Locate platelets.
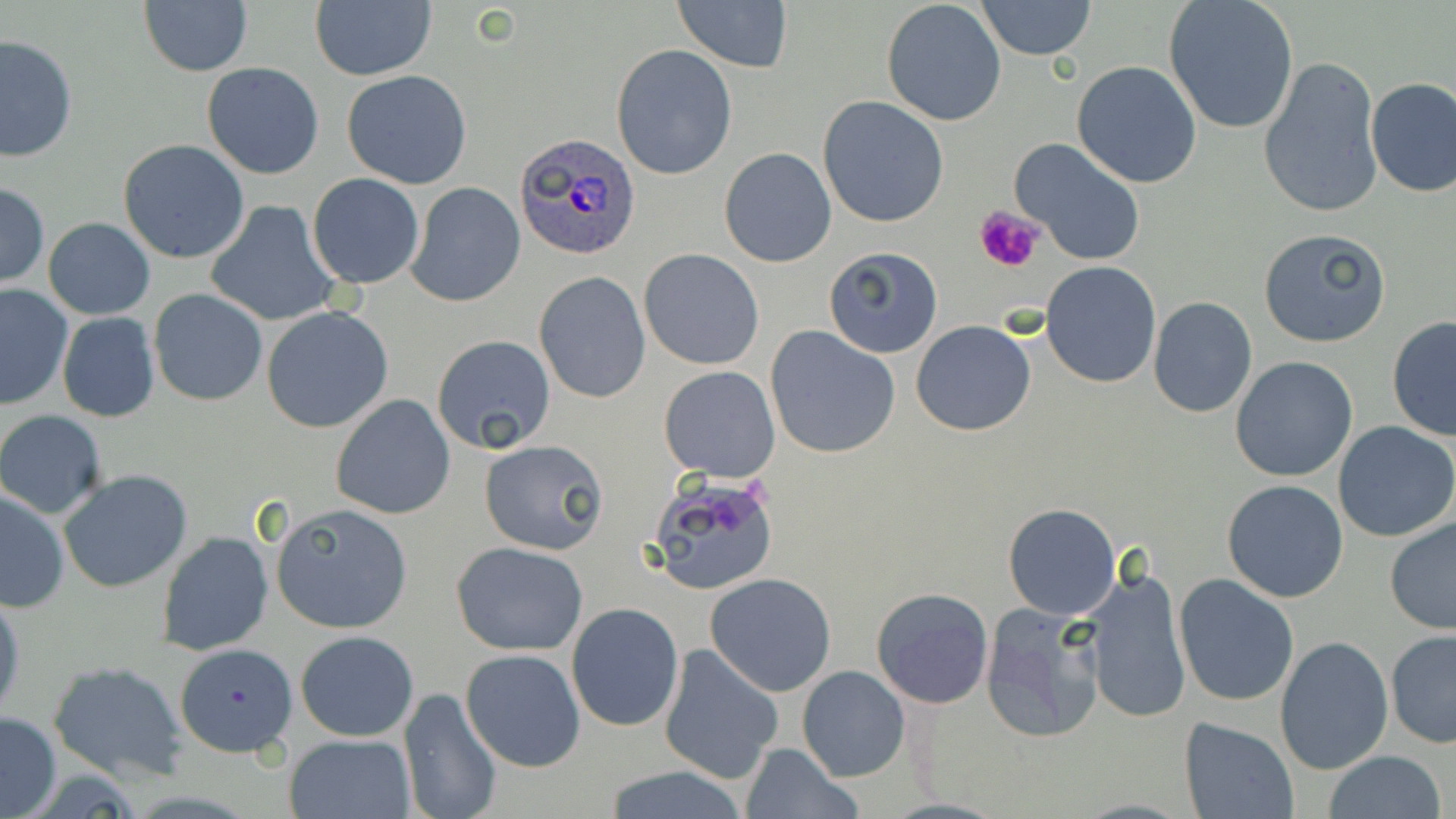
Approximate bounding boxes as (x1, y1, x2, y2) in pixels.
Platelets: (974, 204, 1047, 275).

slide_level_diagnosis: Plasmodium ovale
image_size: 1456×819 pixels
field_of_view: one of a larger specimen
modality: light microscopy
preparation: thin blood smear
stain: May-Grünwald-Giemsa
magnification: 1000x
uninfected_red_blood_cell_locations: 'approximate bounding boxes as (x1, y1, x2, y2) in pixels: (976, 0, 1097, 59), (1162, 0, 1300, 135), (673, 1, 793, 74), (139, 2, 252, 76), (310, 2, 436, 81), (881, 2, 1007, 127), (2, 33, 77, 164), (611, 44, 738, 181), (1072, 60, 1201, 188), (1258, 60, 1382, 216), (202, 61, 324, 179), (343, 69, 472, 190), (1364, 77, 1456, 198), (818, 95, 949, 228), (1011, 138, 1147, 265), (118, 139, 250, 264), (719, 148, 837, 266), (308, 174, 424, 289), (0, 183, 48, 288), (405, 183, 526, 306), (206, 201, 342, 325), (44, 217, 155, 320), (1259, 228, 1391, 349), (824, 247, 945, 358), (639, 248, 763, 370), (1041, 262, 1162, 386), (533, 272, 652, 403), (0, 285, 73, 410), (150, 290, 267, 406), (1147, 296, 1258, 418), (261, 306, 393, 432), (56, 312, 160, 423), (1386, 316, 1456, 443), (912, 321, 1036, 436), (764, 326, 901, 460), (431, 335, 557, 455), (1231, 356, 1359, 482), (659, 365, 781, 482), (330, 395, 456, 520), (0, 410, 107, 518), (1332, 422, 1456, 542), (479, 438, 609, 555), (59, 469, 193, 593), (647, 471, 780, 594), (1221, 480, 1349, 603), (1, 488, 69, 611), (272, 502, 413, 633), (1003, 502, 1121, 621), (1384, 517, 1456, 635), (156, 530, 274, 655), (450, 541, 588, 656), (1077, 567, 1192, 724), (704, 573, 838, 697), (1172, 573, 1299, 707), (869, 587, 995, 709), (0, 589, 24, 725), (566, 603, 684, 732), (978, 603, 1107, 743), (1385, 629, 1456, 748), (296, 630, 420, 741), (1275, 636, 1393, 774), (175, 642, 295, 757), (658, 643, 785, 785), (460, 648, 586, 772), (49, 660, 188, 783), (797, 666, 909, 781), (398, 689, 502, 819), (0, 711, 62, 818), (1179, 717, 1300, 819), (284, 734, 415, 818), (738, 741, 865, 819), (1321, 750, 1448, 819), (602, 764, 752, 819)'
plasmodium_ovale_infected_red_blood_cell_locations: 'approximate bounding boxes as (x1, y1, x2, y2) in pixels: (515, 132, 643, 259)'